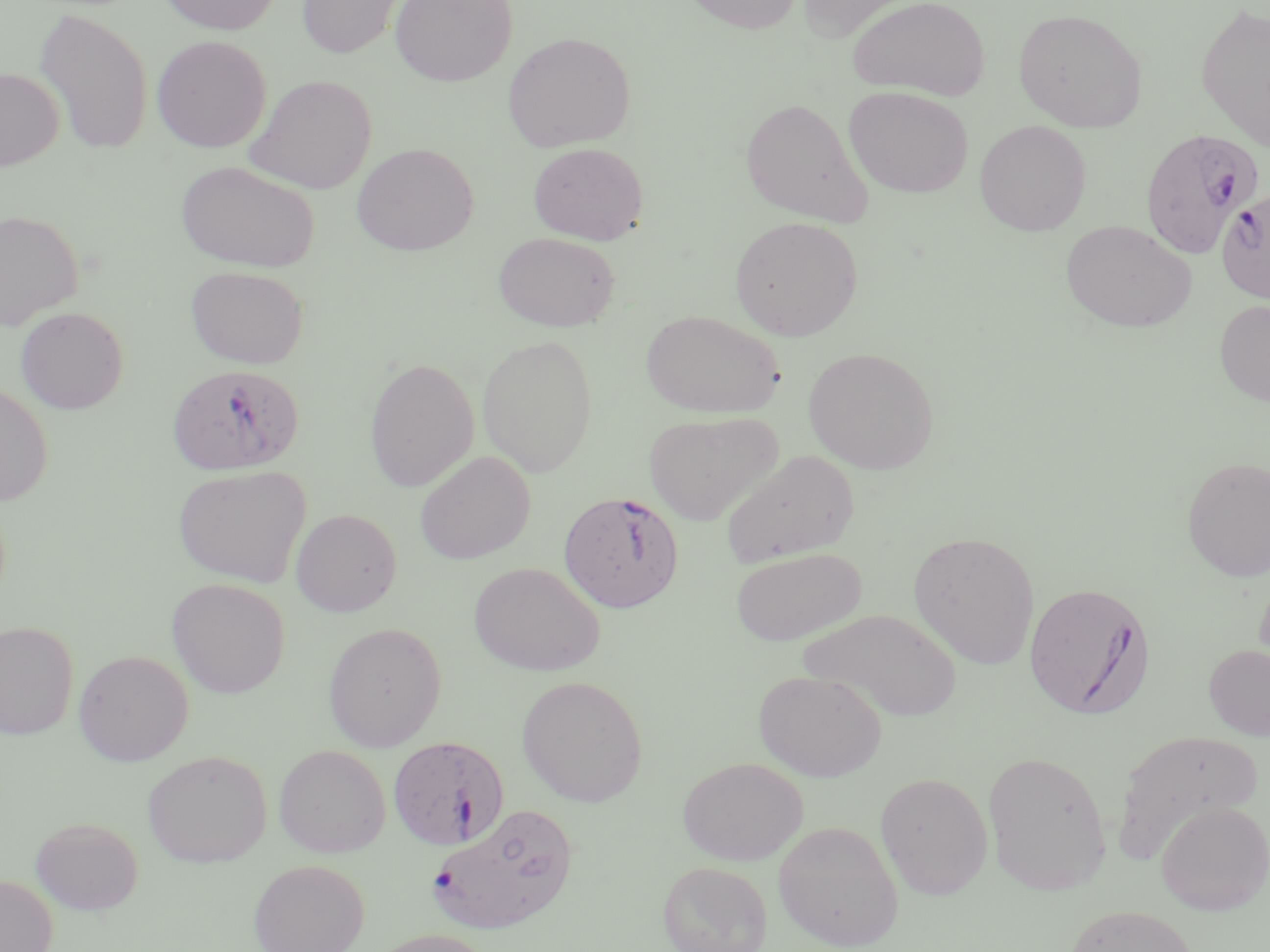

slide-level diagnosis = Plasmodium falciparum
uninfected red blood cell locations = approximate bounding boxes as (x1, y1, x2, y2) in pixels: (158, 0, 282, 35), (296, 0, 407, 60), (390, 0, 518, 87), (678, 0, 804, 35), (794, 0, 926, 43), (848, 0, 990, 102), (1195, 2, 1270, 151), (35, 7, 153, 156), (1013, 8, 1147, 132), (502, 31, 635, 152), (152, 35, 271, 153), (0, 67, 65, 171), (245, 74, 377, 195), (844, 87, 973, 198), (740, 97, 874, 227), (974, 120, 1091, 236), (351, 142, 479, 256), (527, 142, 649, 245), (175, 161, 320, 273), (0, 209, 84, 330), (730, 216, 863, 341), (1060, 219, 1197, 334), (492, 231, 621, 332), (186, 265, 309, 369), (1214, 300, 1270, 407), (15, 306, 128, 414), (640, 309, 785, 419), (477, 334, 598, 478), (802, 346, 939, 474), (364, 357, 479, 493), (0, 382, 53, 506), (643, 411, 784, 526), (720, 450, 859, 566), (415, 451, 536, 564), (1182, 456, 1270, 582), (172, 465, 312, 588), (290, 508, 402, 617), (908, 531, 1041, 669), (730, 547, 867, 646), (469, 562, 605, 676), (1254, 569, 1270, 676), (167, 578, 290, 698), (797, 608, 963, 722), (0, 621, 79, 741), (322, 622, 446, 751), (1203, 644, 1270, 741), (73, 650, 193, 766), (754, 669, 887, 782), (516, 675, 648, 807), (1112, 727, 1265, 861), (274, 744, 391, 858), (143, 750, 272, 867), (983, 750, 1113, 895), (678, 757, 808, 865), (875, 772, 993, 899), (1155, 800, 1270, 915), (30, 816, 144, 915), (772, 820, 904, 950), (248, 859, 370, 952), (658, 860, 772, 952), (0, 874, 58, 952), (1064, 904, 1199, 952), (365, 928, 499, 952)
image size = 1270×952 pixels
stain = May-Grünwald-Giemsa
field of view = single
preparation = thin blood film
magnification = 1000x
Plasmodium falciparum-infected red blood cell locations = approximate bounding boxes as (x1, y1, x2, y2) in pixels: (1139, 127, 1265, 258), (1216, 187, 1270, 305), (166, 363, 303, 476), (558, 490, 685, 614), (1024, 581, 1156, 720), (387, 736, 509, 850), (427, 803, 577, 936)
modality = light microscopy